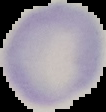
Summary:
  - Image size: 106×112 pixels
  - Preparation: thin blood film
  - Image type: segmented cell region with the area outside set to black
  - Malaria status: uninfected